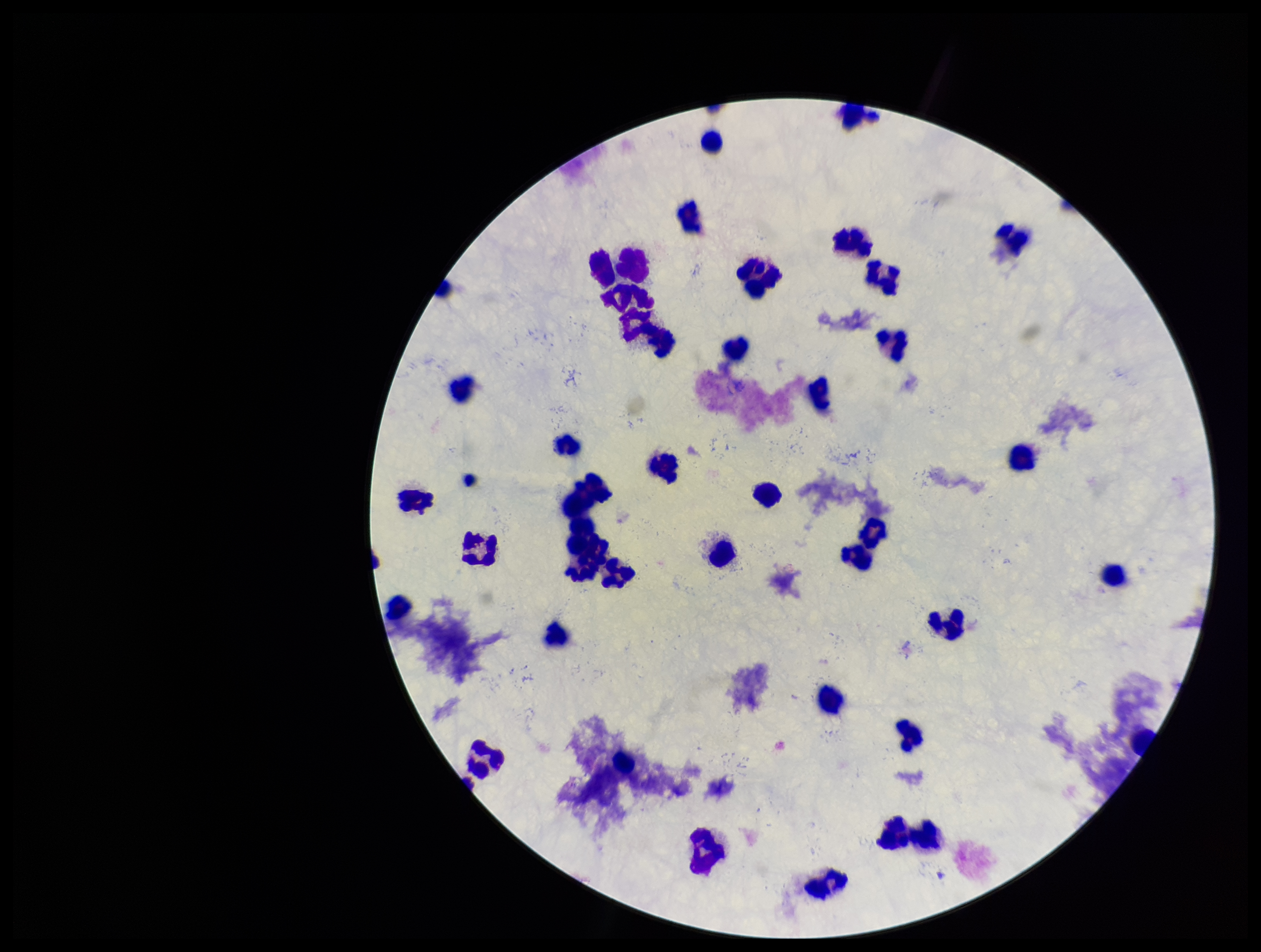
Smartphone photograph taken through the eyepiece of a microscope. Single field of view. Image is 1261×952 pixels. Plasmodium parasites: none detected. Preparation: thick smear. Giemsa stain. Leukocyte count: 38. Parasite count: 0. Patient malaria status: negative.